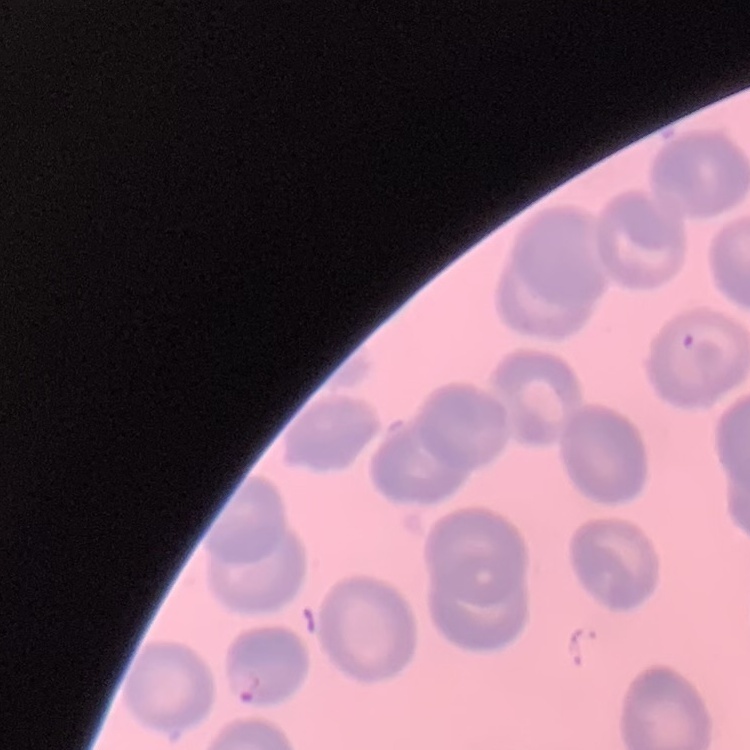
erythrocyte morphology = no rouleaux formation
image type = one tile cut from a larger photomicrograph
preparation = thin blood film
stain = Field's or Giemsa